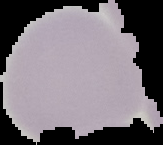
{
  "image_type": "cell region segmented out of the field of view; surrounding area masked to black",
  "malaria_status": "uninfected",
  "preparation": "thin blood film",
  "image_size": "163×145 pixels"
}